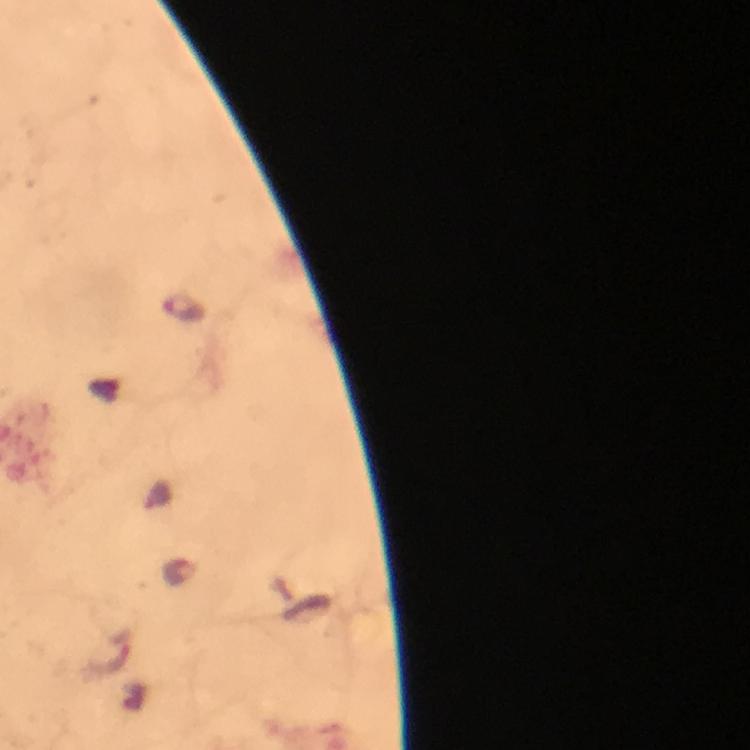

Approximate centers as [x, y] in pixels. Malaria parasite locations: [184, 305]. Thick smear. Image is 750×750 pixels. From a malaria diagnostic workup. Immersion oil applied. Photographed with a smartphone mounted on the microscope. 100x magnification. Cropped region of a single field of view. Giemsa stain.